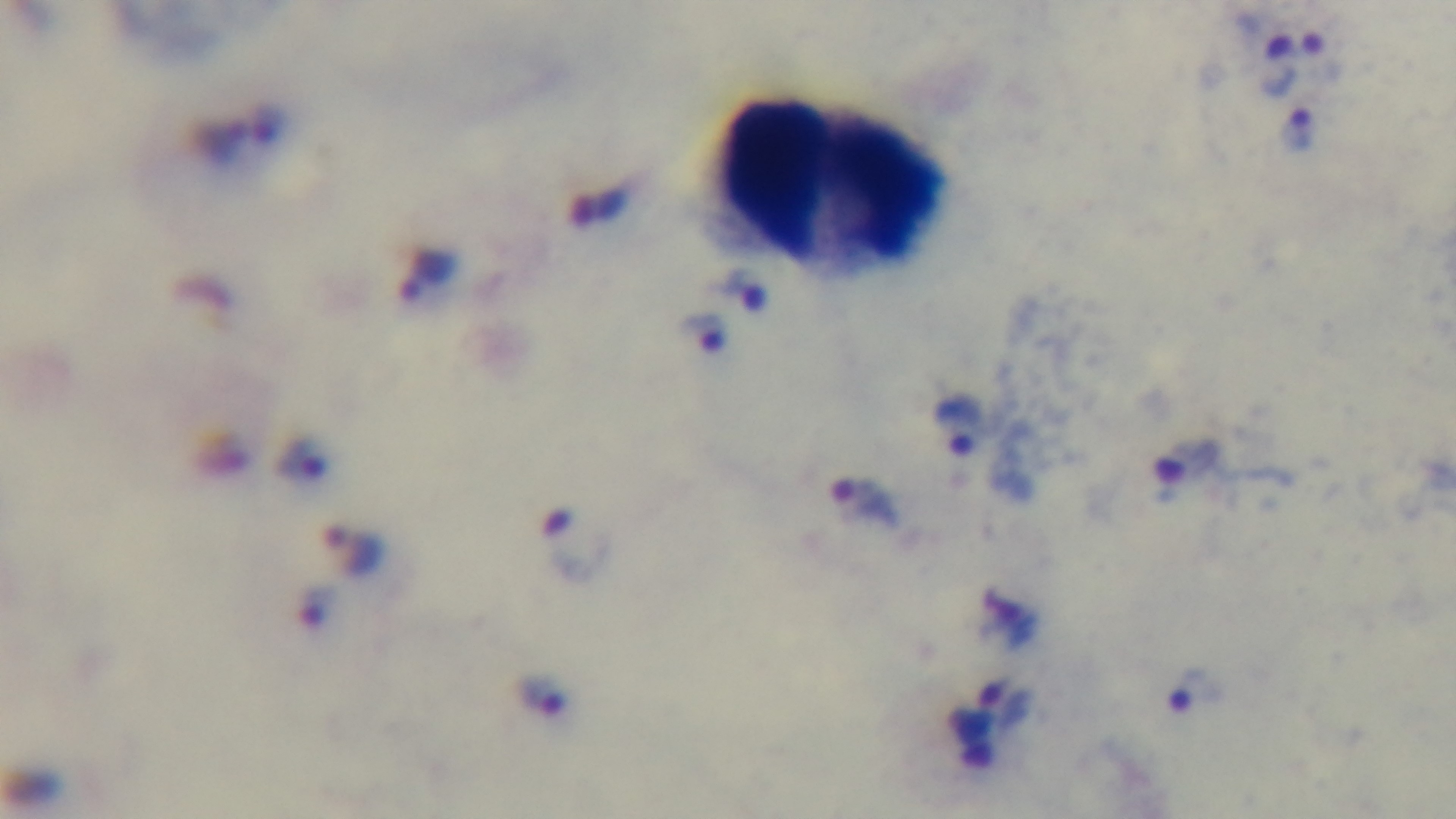

Summary:
  - Capture: mounted 4K digital camera
  - Objective: 100x oil immersion
  - Field of view: single
  - Malaria status: infected
  - Stain: Giemsa
  - Modality: light microscopy
  - Preparation: thick smear